Locate every leukocyte (white blood cell).
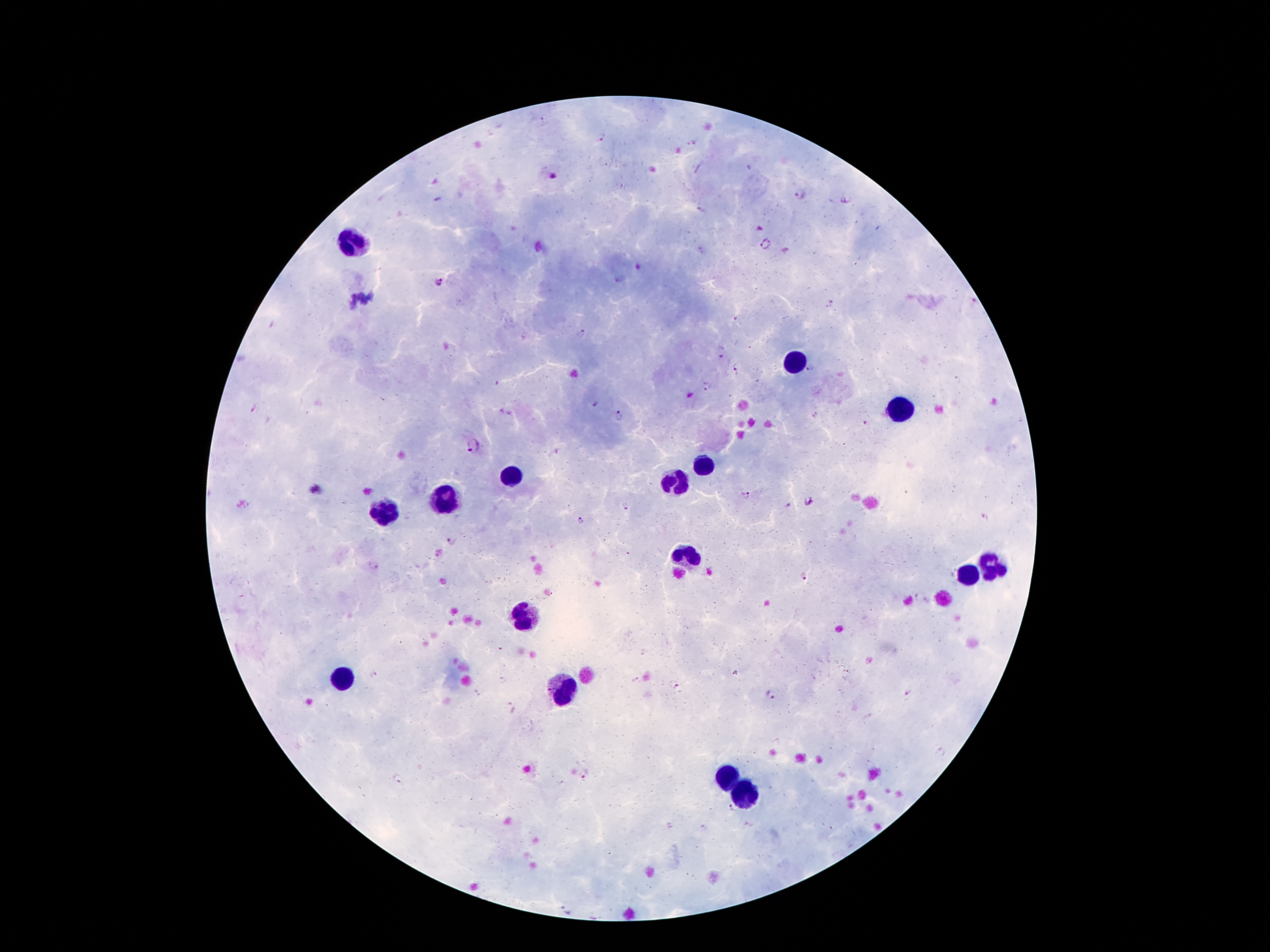

Approximate centers as {x, y} in pixels.
Leukocytes: {353, 243}, {795, 362}, {900, 409}, {708, 468}, {508, 475}, {676, 483}, {448, 502}, {385, 513}, {689, 555}, {991, 569}, {967, 574}, {523, 615}, {342, 679}, {564, 690}, {726, 780}, {747, 795}.

{
  "preparation": "thick blood smear",
  "magnification": "100x",
  "image_size": "1270×952 pixels",
  "malaria_parasite_locations": "approximate centers as {x, y} in pixels: {542, 120}, {602, 139}, {693, 143}, {553, 178}, {801, 194}, {701, 210}, {766, 243}, {442, 282}, {830, 303}, {582, 333}, {722, 358}, {736, 365}, {808, 369}, {706, 385}, {620, 416}, {865, 423}, {473, 446}, {316, 489}, {747, 495}, {809, 501}, {788, 505}, {626, 507}, {580, 521}, {452, 540}, {802, 576}, {673, 685}, {770, 694}, {398, 780}, {731, 810}, {567, 910}",
  "stain": "Giemsa",
  "patient_malaria_status": "infected with Plasmodium falciparum",
  "field_of_view": "one from this slide",
  "capture": "smartphone through the microscope eyepiece"
}